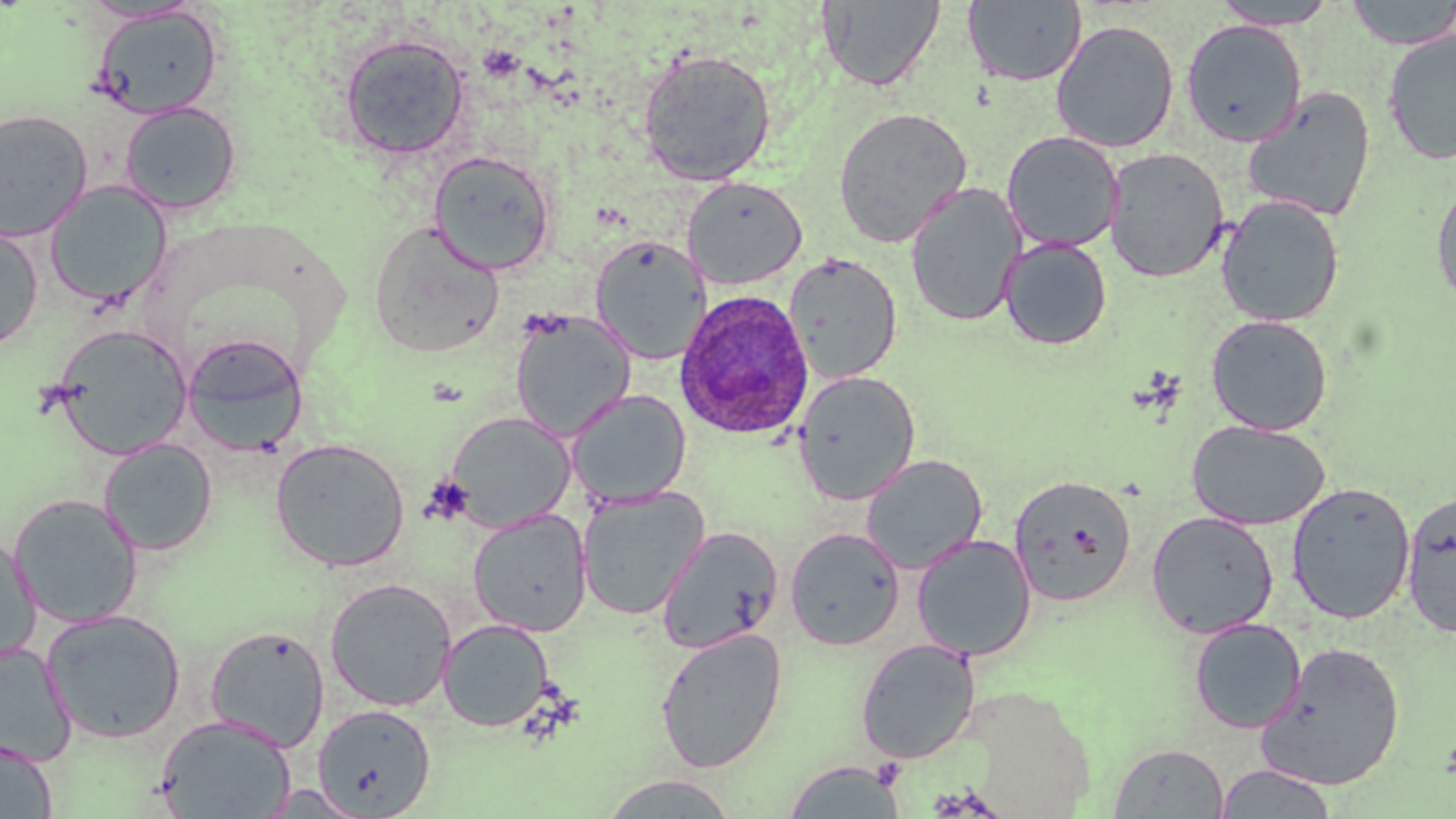
Summary:
  - Coordinate format: approximate bounding boxes as (x1,y1)-(x2,y2) corner pairs in pixels
  - Plasmodium ovale-infected red blood cell locations: (674,290)-(815,441)
  - Uninfected red blood cell locations: (1343,0)-(1456,49), (819,1)-(946,92), (962,1)-(1087,86), (1210,1)-(1340,29), (90,5)-(224,119), (1050,19)-(1180,153), (1180,19)-(1307,147), (1382,29)-(1456,165), (338,33)-(471,161), (638,48)-(777,187), (1241,87)-(1377,223), (120,102)-(241,215), (833,106)-(973,247), (0,109)-(94,242), (1001,131)-(1124,253), (1103,147)-(1230,283), (428,150)-(556,276), (682,176)-(807,290), (1430,177)-(1456,310), (44,181)-(172,308), (904,181)-(1026,327), (1216,195)-(1346,327), (368,220)-(506,359), (0,225)-(43,353), (589,236)-(710,364), (999,237)-(1112,350), (785,252)-(903,384), (510,309)-(636,440), (1205,314)-(1333,435), (48,325)-(193,460), (181,333)-(309,456), (793,369)-(920,505), (567,388)-(691,508), (444,410)-(576,531), (1187,420)-(1331,530), (270,437)-(410,572), (98,438)-(218,556), (860,454)-(987,574), (1009,474)-(1138,607), (1286,481)-(1416,624), (577,487)-(709,620), (1399,489)-(1456,640), (9,493)-(143,628), (468,510)-(592,637), (1145,510)-(1279,638), (657,525)-(784,654), (785,527)-(905,651), (1,531)-(41,666), (912,534)-(1037,661), (325,578)-(457,711), (41,609)-(187,743), (438,618)-(555,732), (1188,618)-(1306,733), (204,625)-(329,751), (654,627)-(787,773), (855,638)-(981,764), (1258,641)-(1406,790), (0,642)-(77,766), (312,703)-(436,817), (155,714)-(296,819), (0,736)-(57,819), (1108,742)-(1230,818), (782,760)-(908,818), (1214,764)-(1338,818), (598,773)-(741,817)
  - Slide-level diagnosis: Plasmodium ovale
  - Magnification: 1000x
  - Stain: May-Grünwald-Giemsa
  - Preparation: thin blood film
  - Field of view: single
  - Modality: optical microscopy
  - Image size: 1456×819 pixels